State which parasite is depicted.
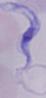
This is a trypanosome.

1000x magnification. Micrograph.